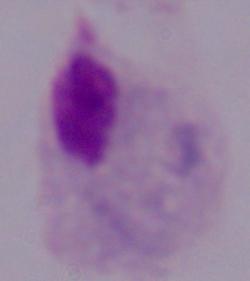
Summary:
  - Identification: trichomonad
  - Modality: photomicrograph
  - Magnification: 1000x